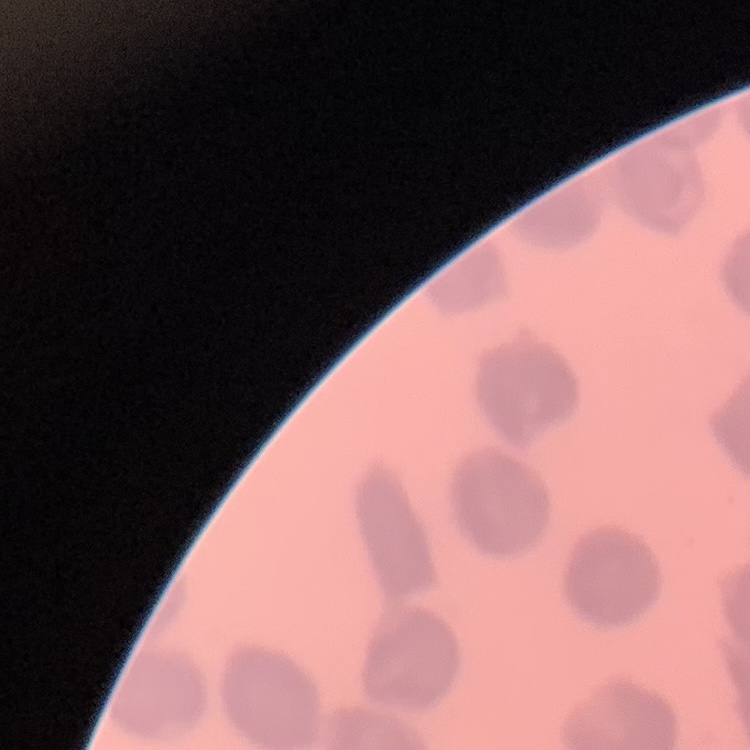
{
  "erythrocyte_morphology": "no rouleaux formation",
  "stain": "Field's or Giemsa",
  "image_type": "one tile cut from a larger photomicrograph",
  "preparation": "thin blood film"
}